Classify this cell by malaria status.
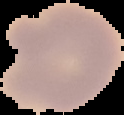

It is uninfected.

Summary:
  - Image type: cell region segmented out of the field of view; surrounding area masked to black
  - Image size: 124×115 pixels
  - Preparation: thin blood film